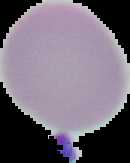 From a thin blood film. Segmented cell region on a black background. Malaria status: uninfected. Image is 130×163 pixels.